State which parasite is depicted.
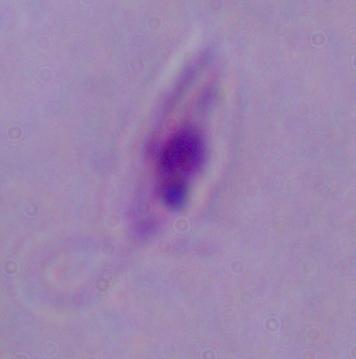
This is Leishmania.

Summary:
  - Modality: photomicrograph
  - Magnification: 1000x